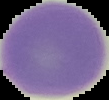
image_size: 109×100 pixels
result: negative for Plasmodium parasites
preparation: thin blood film
image_type: segmented cell region on a black background